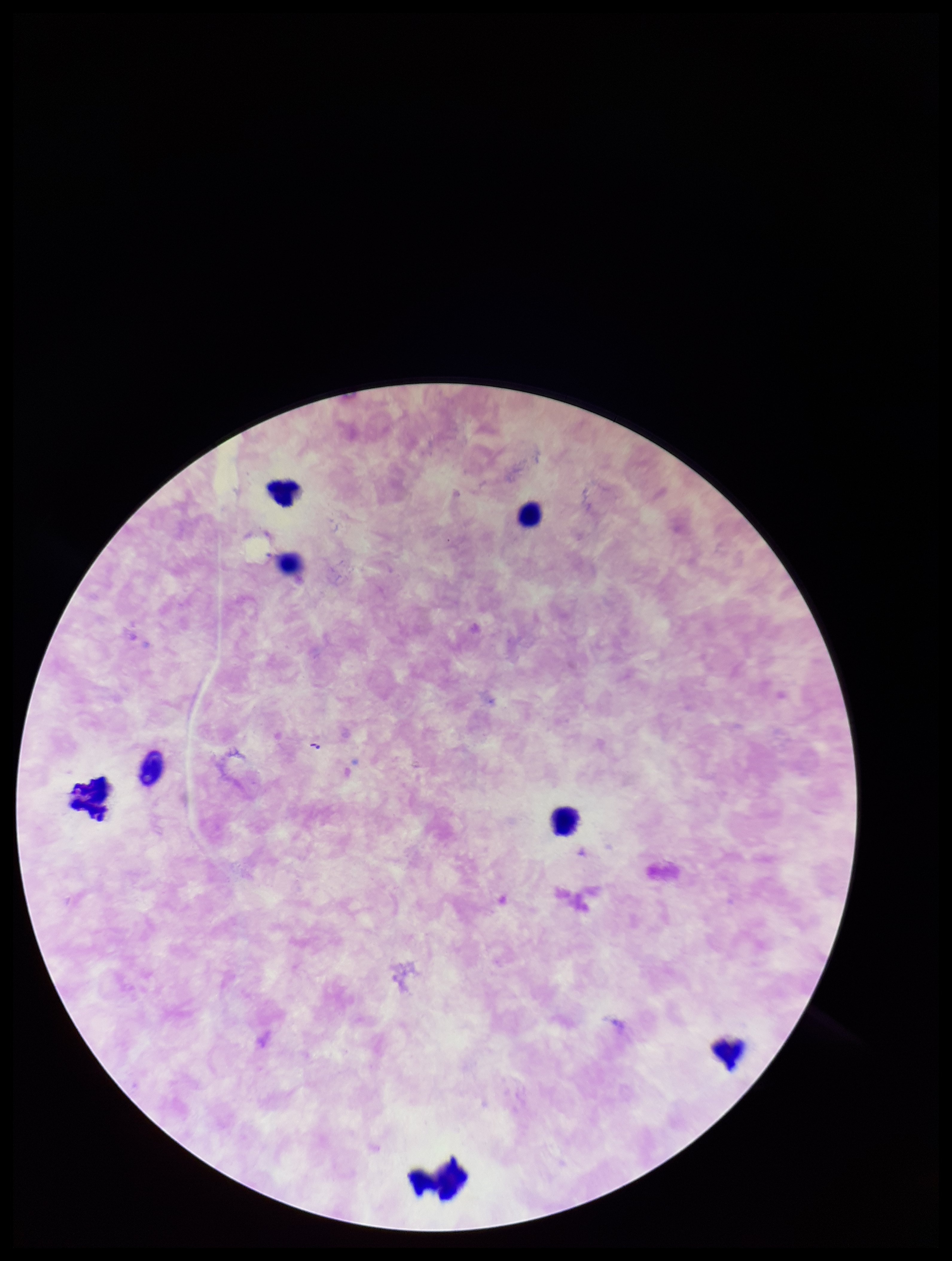

Photographed through the microscope eyepiece with a smartphone camera. Image is 952×1261 pixels. Preparation: thick smear. Single field of view. Leukocyte count: 8. Species reported for this patient: Plasmodium falciparum. Patient malaria status: positive. Stained with Giemsa. Plasmodium parasites: none seen. Parasite count: 0.